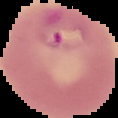
{
  "image_type": "cell region segmented out of the field of view; surrounding area masked to black",
  "result": "Plasmodium parasites detected",
  "preparation": "thin blood smear",
  "image_size": "118×118 pixels"
}